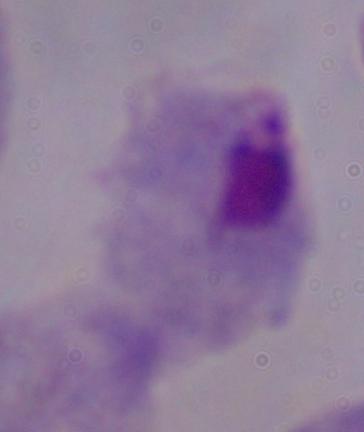
{
  "magnification": "1000x",
  "identification": "trichomonad",
  "modality": "micrograph"
}